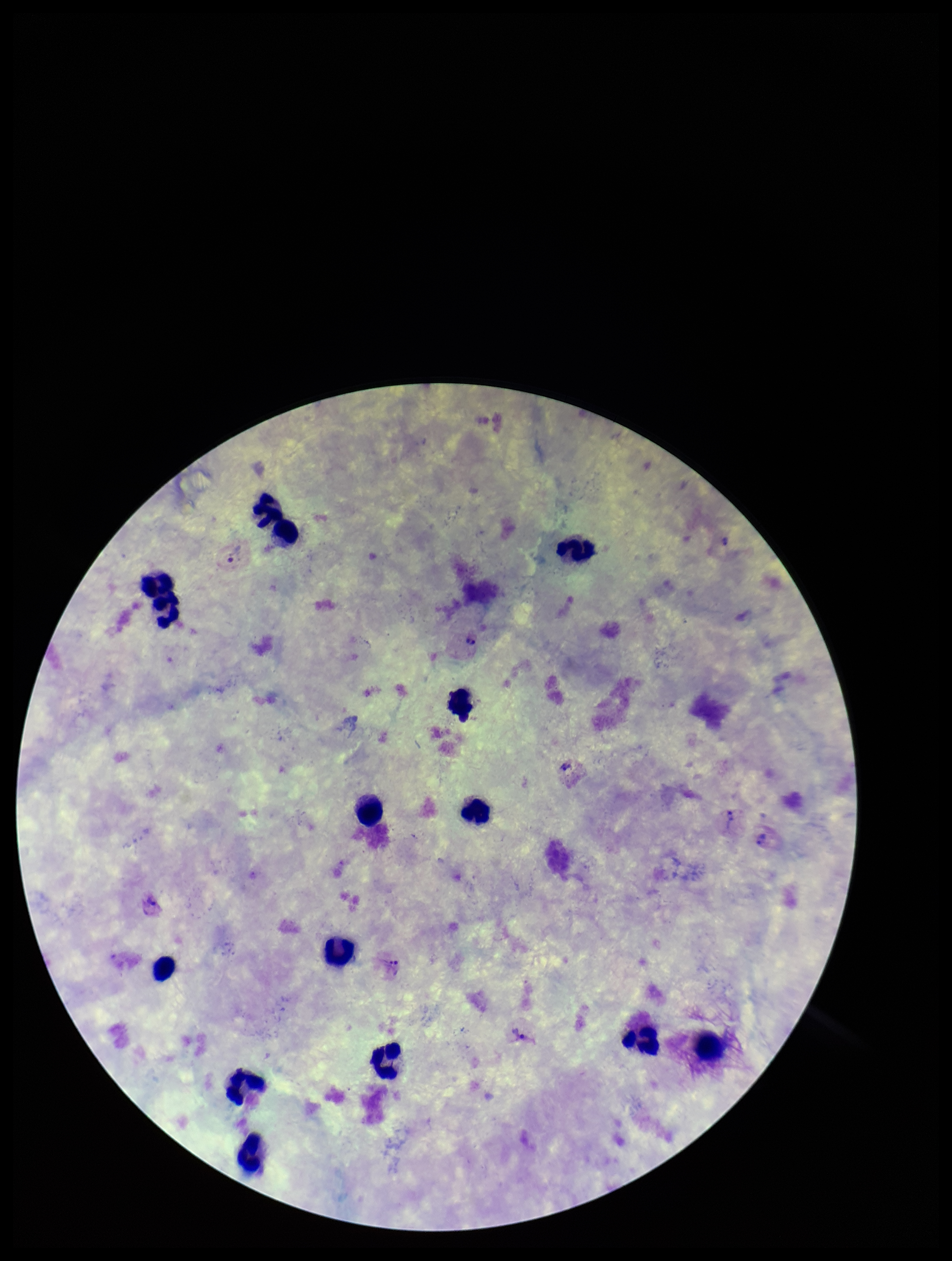
patient_malaria_status: infected
parasite_count: 3
leukocyte_count: 14
preparation: thick blood smear
stain: Giemsa
field_of_view: one from this slide
plasmodium_parasites: detected
image_size: 952×1261 pixels
capture: smartphone photograph through the microscope eyepiece
species_reported_for_this_patient: Plasmodium vivax